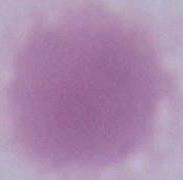
Captured at 1000x magnification. Micrograph. A red blood cell is seen.